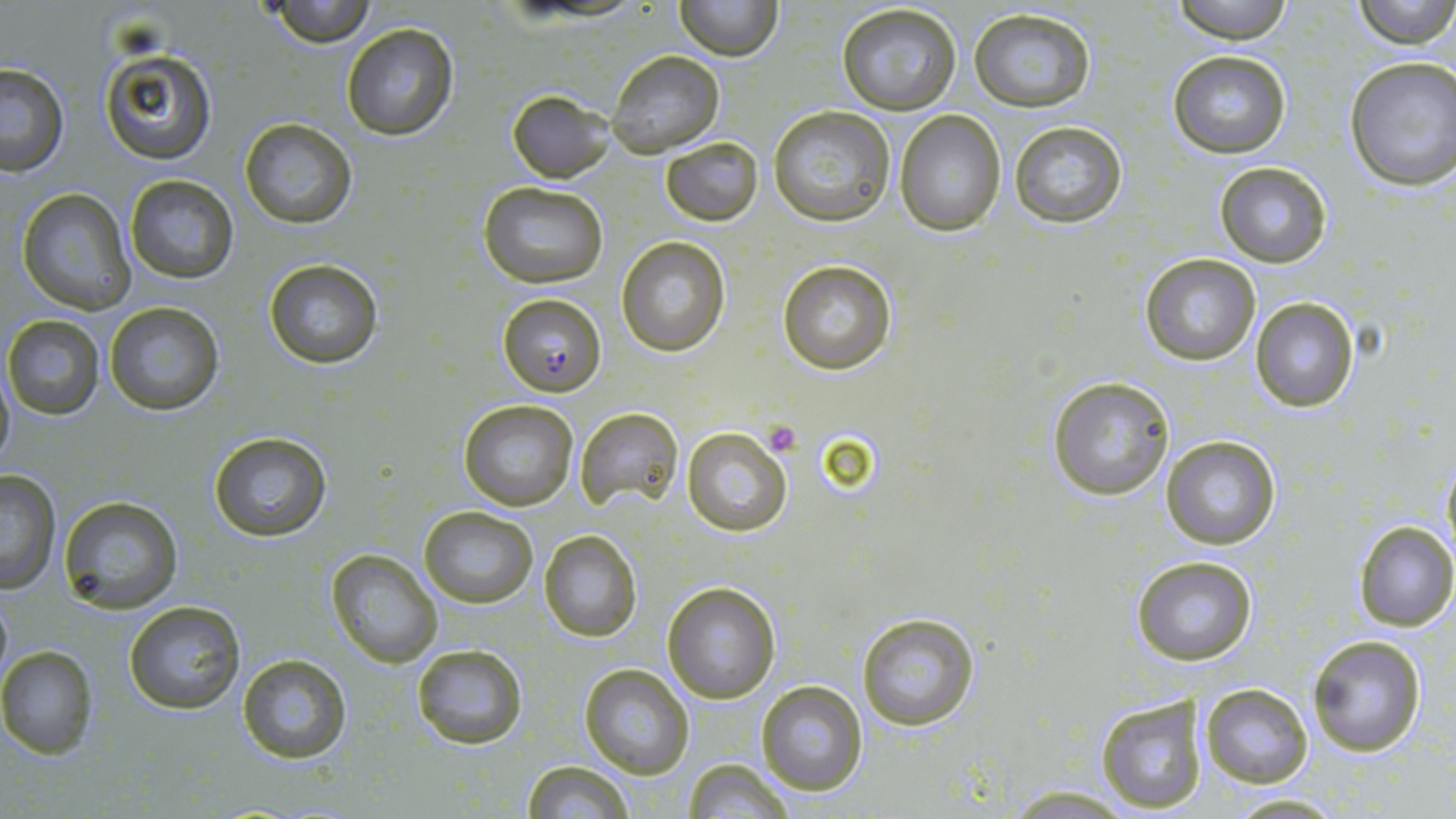 Approximate bounding boxes as (x1,y1)-(x2,y2) corner pairs in pixels. Plasmodium falciparum-infected red blood cell locations: (497,292)-(606,397). Uninfected red blood cell locations: (675,0)-(782,60), (1170,0)-(1294,42), (1354,0)-(1455,48), (263,1)-(382,47), (836,3)-(962,115), (969,7)-(1096,112), (341,21)-(460,141), (98,47)-(217,165), (606,51)-(724,156), (1169,51)-(1291,158), (1345,56)-(1456,192), (0,64)-(71,176), (508,90)-(616,183), (768,107)-(896,227), (894,111)-(1007,236), (239,118)-(358,228), (1008,120)-(1127,227), (661,138)-(762,225), (1215,163)-(1332,267), (125,174)-(239,284), (479,181)-(609,290), (17,187)-(137,315), (616,238)-(730,356), (1140,253)-(1260,367), (263,258)-(384,370), (776,260)-(896,375), (1250,297)-(1360,414), (103,302)-(227,417), (3,314)-(108,420), (0,368)-(14,479), (1048,376)-(1176,500), (458,398)-(579,512), (573,407)-(683,515), (681,425)-(794,537), (207,430)-(332,543), (1162,435)-(1281,550), (1440,458)-(1456,563), (0,471)-(61,592), (57,496)-(184,613), (420,508)-(539,607), (1354,521)-(1456,631), (539,530)-(641,641), (326,549)-(443,669), (1132,555)-(1258,666), (662,581)-(781,702), (0,587)-(13,696), (123,600)-(248,716), (857,611)-(981,732), (1308,634)-(1428,756), (410,644)-(528,749), (0,645)-(99,757), (236,652)-(353,765), (580,664)-(694,778), (755,680)-(868,797), (1200,685)-(1312,787), (1094,690)-(1211,813), (680,758)-(795,818), (523,760)-(634,818), (999,785)-(1137,815), (1221,793)-(1351,817). Platelet locations: (762,421)-(800,454). Slide-level diagnosis: Plasmodium falciparum. Image is 1456×819 pixels. 1000x magnification. Single field of view. May-Grünwald-Giemsa-stained preparation. Thin blood smear. Light microscopy.